Name the parasite shown.
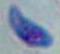

This is Toxoplasma gondii.

modality: micrograph
magnification: 1000x